Assess the morphology of the red blood cells.
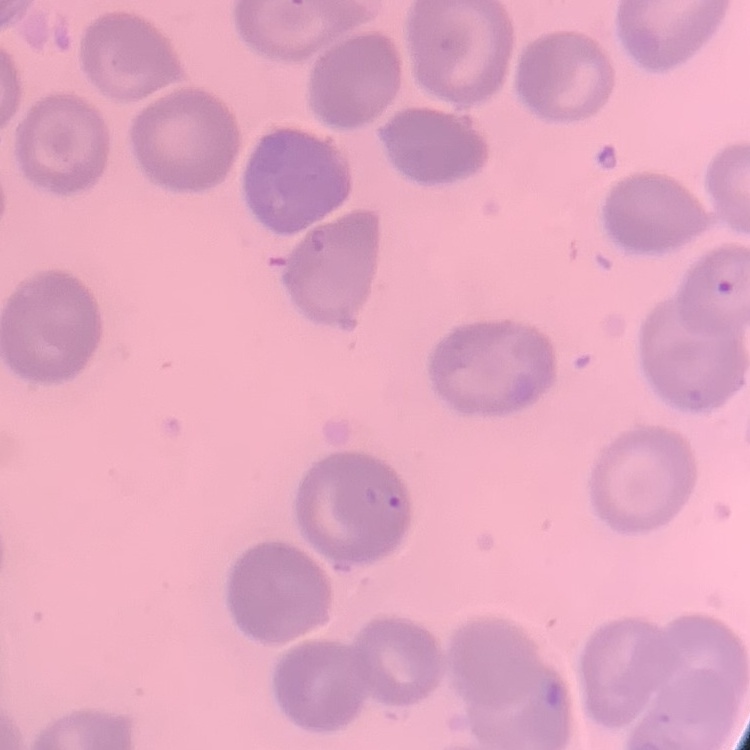

They show no rouleaux formation.

One tile cut from a larger photomicrograph. Thin blood smear. Stained with either Field's or Giemsa.